Locate every Plasmodium malariae-infected red blood cell.
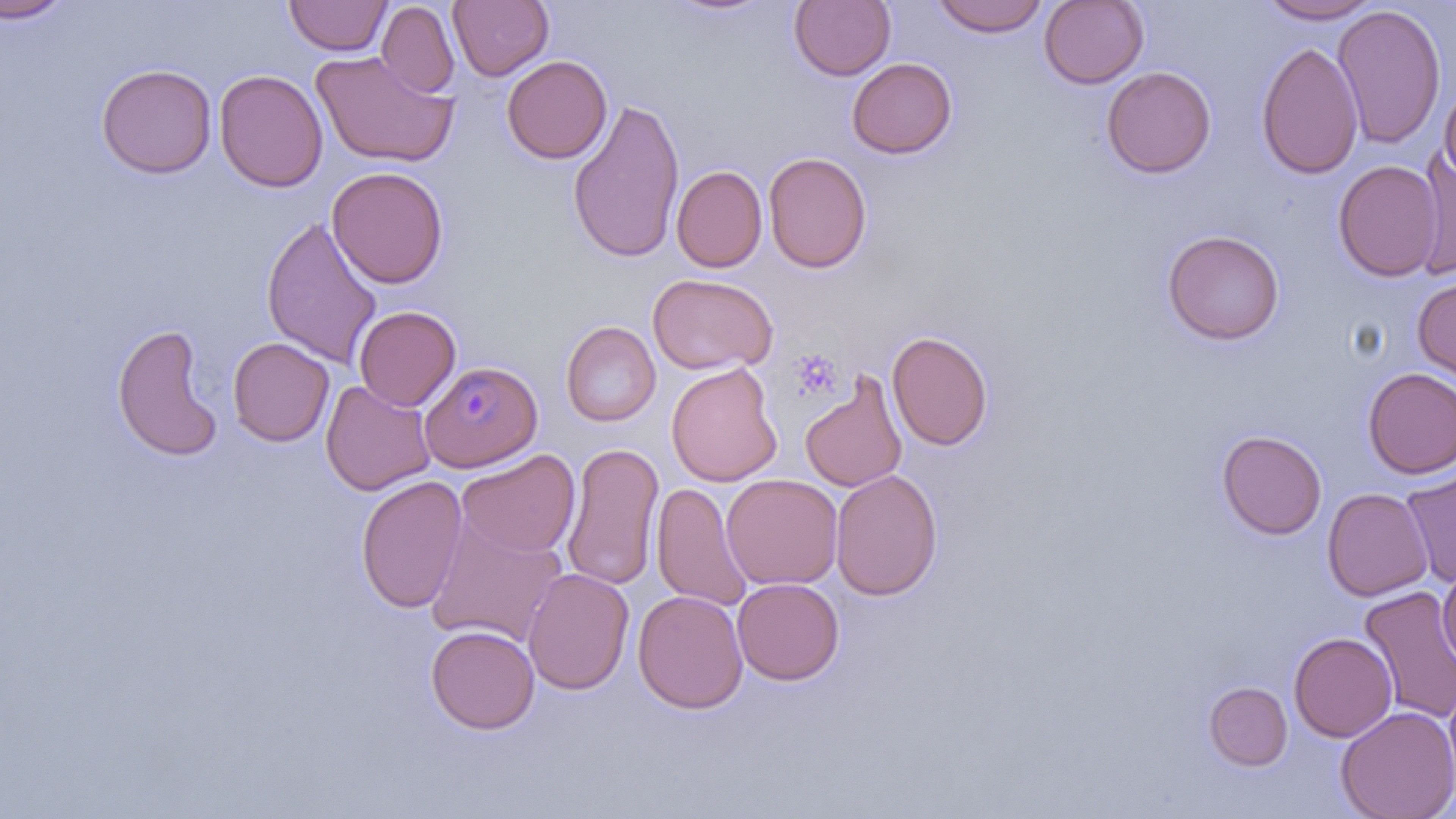

Approximate bounding boxes as [x1, y1, x2, y2] in pixels.
Plasmodium malariae-infected red blood cells: [421, 360, 542, 471].

Uninfected red blood cell locations: [0, 0, 73, 24], [284, 0, 392, 56], [788, 0, 896, 81], [929, 0, 1050, 37], [1039, 0, 1149, 89], [1255, 0, 1382, 24], [448, 1, 553, 81], [377, 2, 459, 99], [1332, 3, 1447, 151], [1256, 41, 1363, 180], [311, 50, 459, 168], [502, 55, 612, 164], [847, 57, 957, 159], [96, 63, 218, 178], [1102, 66, 1216, 178], [214, 69, 328, 193], [1439, 79, 1456, 187], [567, 98, 685, 264], [1413, 148, 1456, 282], [763, 152, 872, 273], [1333, 160, 1443, 282], [671, 165, 767, 273], [327, 167, 449, 288], [261, 216, 383, 368], [1162, 228, 1285, 345], [647, 272, 776, 375], [1413, 276, 1456, 388], [354, 305, 461, 411], [560, 321, 661, 426], [110, 322, 225, 463], [887, 331, 993, 451], [227, 336, 334, 447], [666, 362, 783, 487], [1361, 368, 1456, 478], [800, 371, 909, 493], [321, 379, 436, 496], [1216, 429, 1327, 540], [561, 442, 665, 591], [456, 449, 580, 559], [830, 469, 943, 600], [1400, 470, 1456, 588], [722, 474, 843, 591], [355, 475, 468, 614], [652, 482, 754, 613], [1322, 488, 1433, 600], [424, 513, 568, 649], [522, 567, 635, 695], [1438, 568, 1456, 670], [732, 578, 844, 685], [1359, 586, 1456, 725], [632, 590, 748, 714], [426, 625, 540, 734], [1289, 632, 1397, 742], [1444, 681, 1456, 794], [1204, 682, 1292, 771], [1336, 705, 1456, 819]. Slide-level diagnosis: Plasmodium malariae. Thin blood film. Captured at 1000x magnification. May-Grünwald-Giemsa stain. Single field of view. Optical microscopy. Image is 1456×819 pixels.